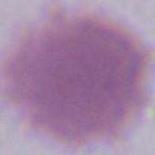

magnification = 1000x
modality = photomicrograph
identification = erythrocyte